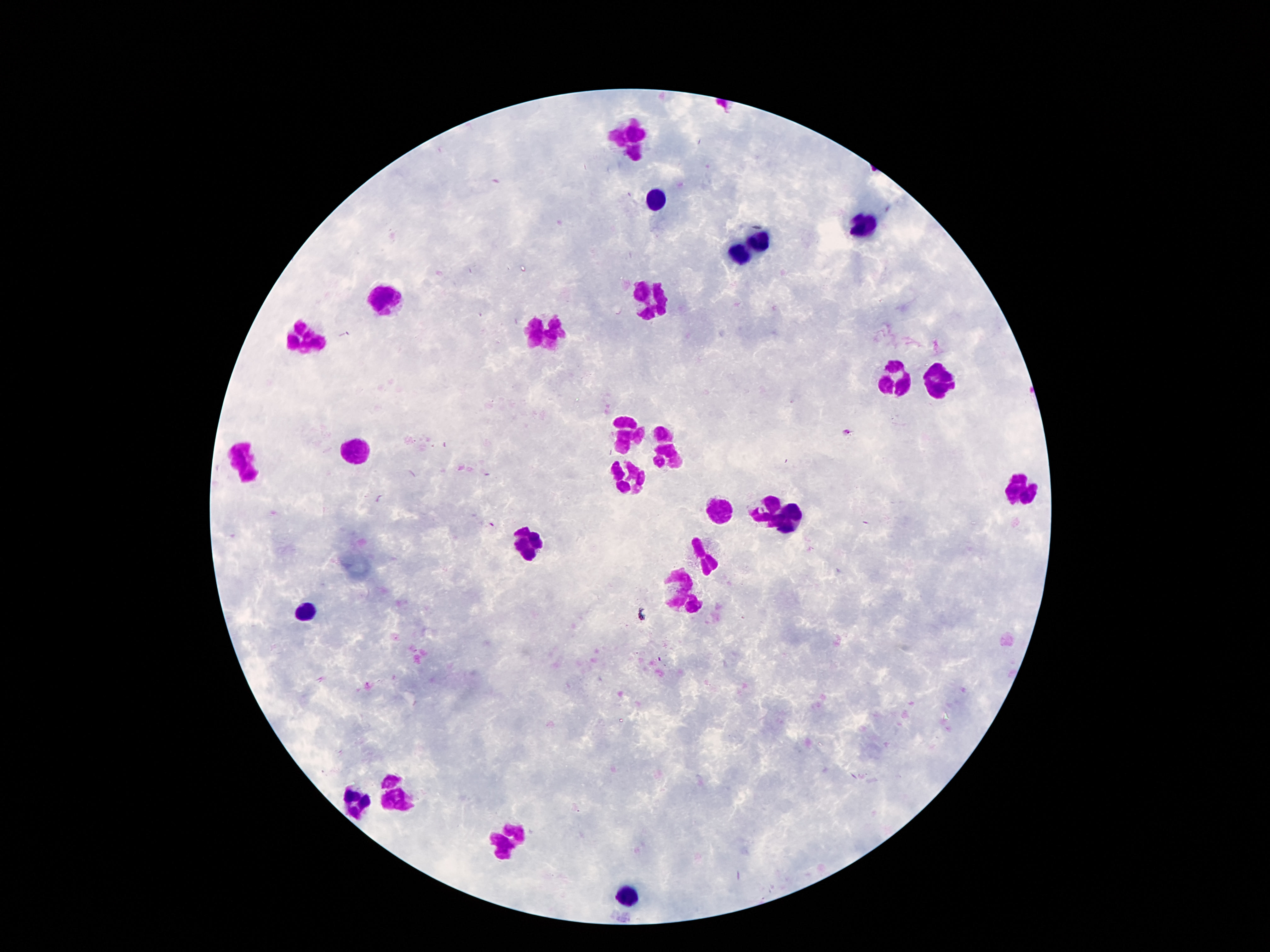

{
  "capture": "smartphone camera through the microscope eyepiece",
  "leukocyte_locations": "approximate centers as (x, y) in pixels: (630, 134), (653, 199), (861, 227), (762, 239), (739, 256), (382, 299), (653, 302), (550, 333), (309, 337), (943, 381), (897, 383), (624, 428), (659, 432), (359, 451), (666, 456), (242, 463), (628, 476), (1019, 489), (767, 510), (720, 511), (792, 520), (527, 543), (710, 554), (678, 585), (311, 609), (402, 792), (356, 800), (505, 841), (622, 898)",
  "stain": "Giemsa",
  "preparation": "thick peripheral-blood smear",
  "field_of_view": "single",
  "patient_malaria_status": "not infected",
  "image_size": "1270×952 pixels",
  "magnification": "100x"
}